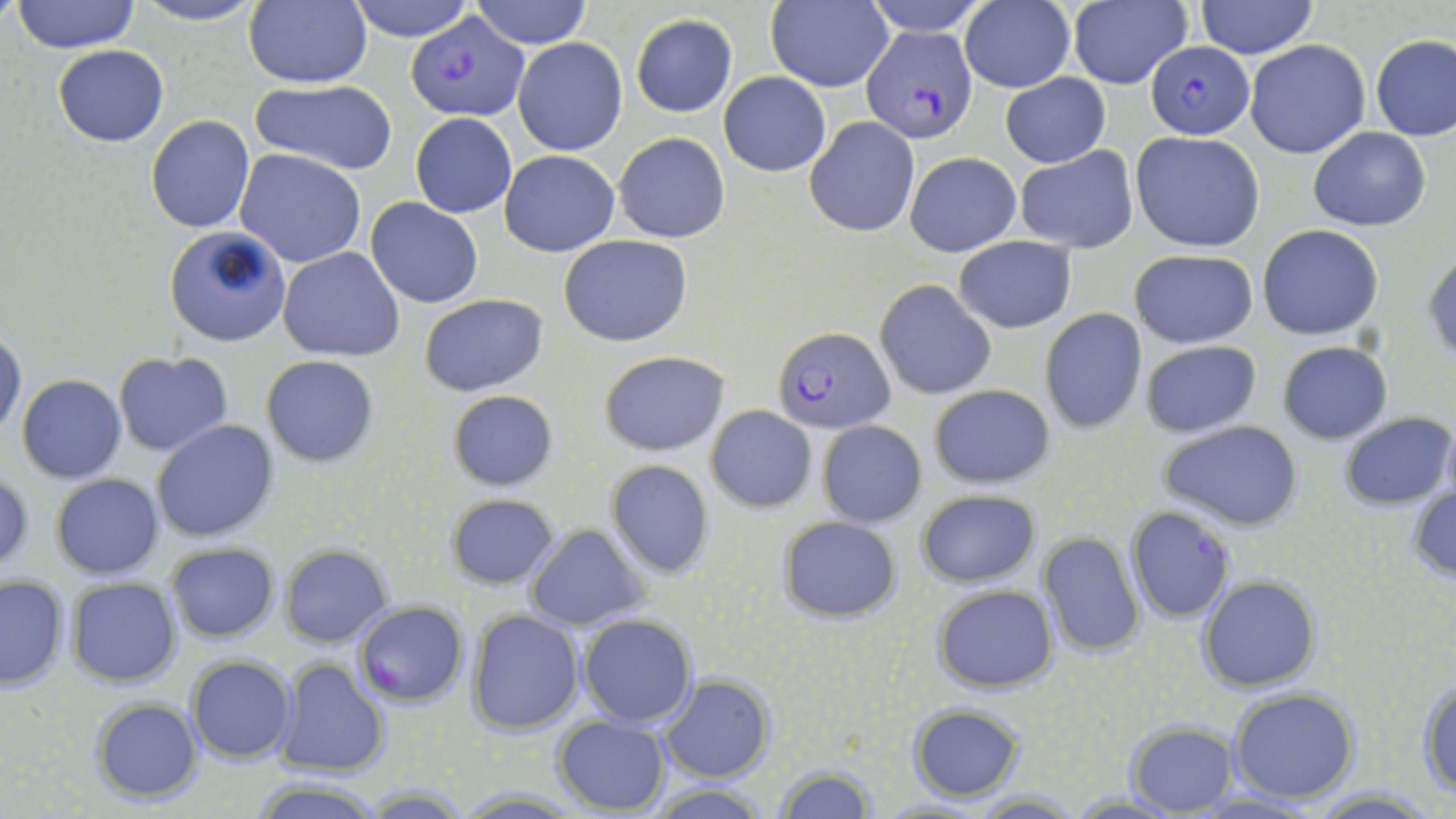
Approximate bounding boxes as [x1, y1, x2, y2] in pixels. Plasmodium falciparum-infected red blood cell locations: [405, 13, 527, 121], [863, 26, 978, 141], [1146, 40, 1254, 138], [770, 327, 895, 433], [1126, 506, 1234, 622]. Uninfected red blood cell locations: [131, 0, 265, 27], [346, 0, 477, 42], [468, 0, 594, 49], [764, 0, 893, 91], [861, 0, 990, 37], [1194, 0, 1320, 58], [12, 1, 141, 52], [242, 1, 373, 89], [959, 2, 1074, 92], [1066, 2, 1190, 90], [629, 14, 739, 117], [1371, 34, 1456, 141], [513, 37, 626, 156], [1245, 40, 1370, 158], [53, 45, 169, 146], [718, 72, 829, 176], [1000, 73, 1110, 168], [250, 77, 399, 176], [409, 112, 517, 218], [146, 114, 255, 234], [805, 117, 919, 237], [1308, 127, 1431, 231], [1130, 130, 1265, 252], [612, 132, 730, 243], [1015, 145, 1139, 254], [235, 149, 366, 267], [499, 150, 619, 257], [905, 151, 1021, 256], [367, 197, 484, 308], [1257, 225, 1384, 340], [164, 226, 291, 347], [558, 235, 693, 347], [953, 237, 1077, 333], [278, 247, 404, 361], [1128, 249, 1258, 347], [1425, 250, 1456, 364], [875, 279, 997, 399], [420, 293, 548, 397], [1037, 309, 1147, 433], [0, 332, 25, 440], [1139, 339, 1262, 438], [1277, 341, 1391, 444], [599, 350, 728, 455], [114, 351, 232, 457], [262, 356, 379, 467], [16, 374, 126, 484], [928, 383, 1056, 490], [447, 390, 559, 491], [705, 404, 817, 512], [1338, 412, 1454, 509], [151, 419, 279, 543], [817, 420, 927, 528], [1158, 421, 1302, 531], [606, 460, 715, 578], [0, 472, 33, 573], [51, 474, 164, 580], [1407, 481, 1456, 583], [916, 490, 1040, 589], [446, 493, 560, 590], [776, 514, 902, 623], [526, 524, 650, 631], [1037, 531, 1146, 658], [166, 542, 280, 643], [280, 544, 393, 647], [0, 575, 69, 691], [1198, 575, 1321, 693], [66, 576, 183, 687], [932, 584, 1058, 695], [354, 601, 470, 706], [466, 610, 584, 734], [577, 614, 698, 728], [185, 656, 296, 764], [275, 658, 389, 778], [660, 676, 772, 784], [1417, 677, 1456, 796], [1228, 688, 1359, 804], [90, 698, 202, 804], [908, 704, 1025, 801], [552, 715, 670, 814], [1124, 723, 1235, 815], [772, 765, 878, 817], [249, 777, 383, 817], [647, 783, 774, 818], [1304, 786, 1443, 817], [451, 788, 584, 816], [971, 791, 1083, 817], [1067, 793, 1184, 818], [874, 798, 995, 818]. Slide-level diagnosis: Plasmodium falciparum. Captured at 1000x magnification. Optical microscopy. Single field of view. Image is 1456×819 pixels. Thin blood smear. May-Grünwald-Giemsa-stained preparation.